Identify the parasite.
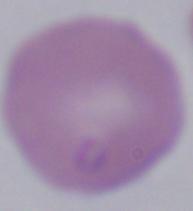

Babesia.

modality: micrograph
magnification: 1000x